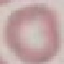
result = negative for malaria parasites
capture = smartphone camera at the microscope eyepiece
preparation = thin blood smear
image type = automatically extracted cell patch, resized to 64 × 64 pixels
stain = Giemsa